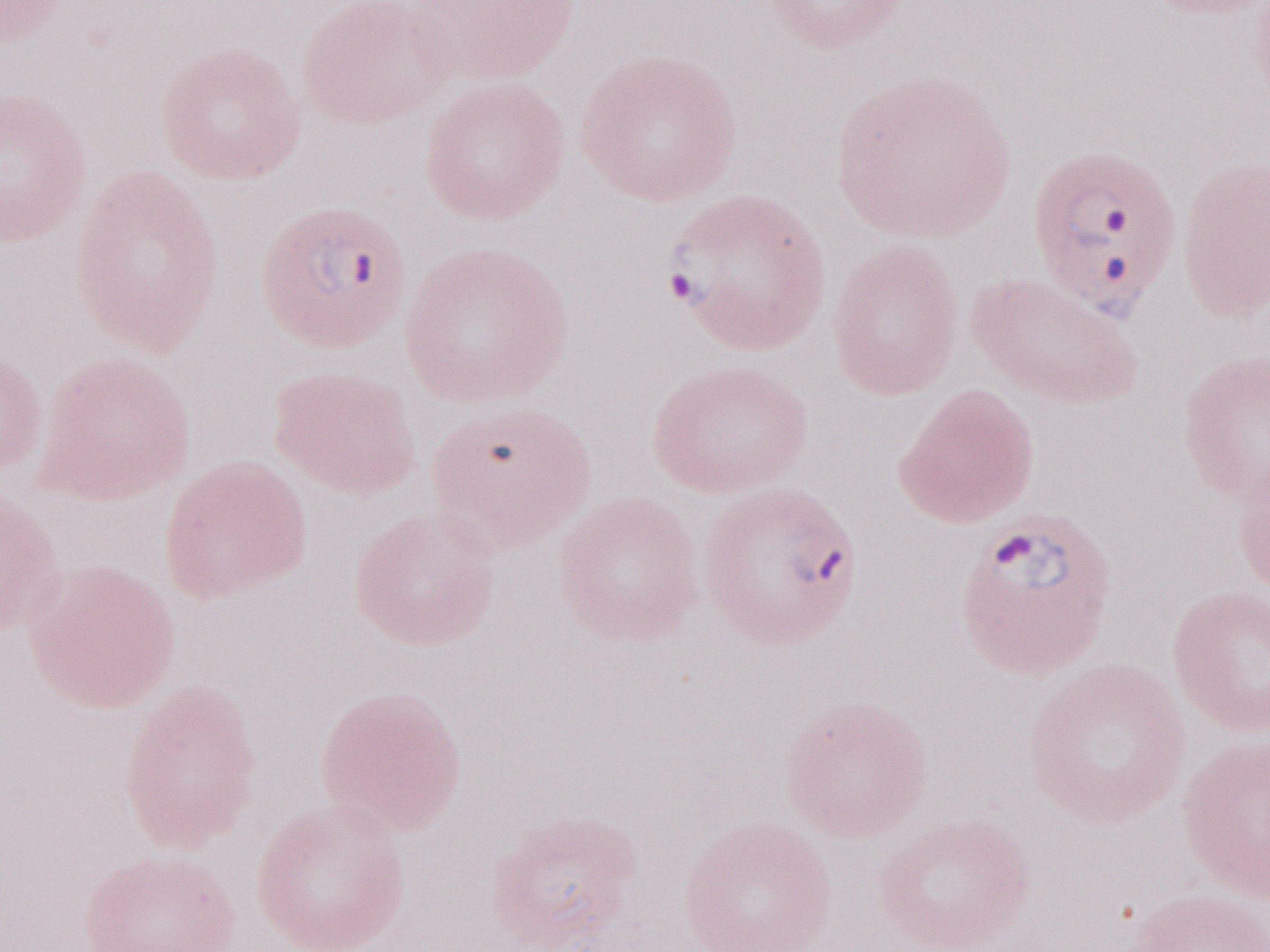
Single field of view. May-Grünwald-Giemsa-stained preparation. Thin blood smear. Magnification: 1,000x. Image is 1270×952 pixels. Patient-level malaria diagnosis: positive. Olympus BX43 microscope, Olympus DP73 camera.